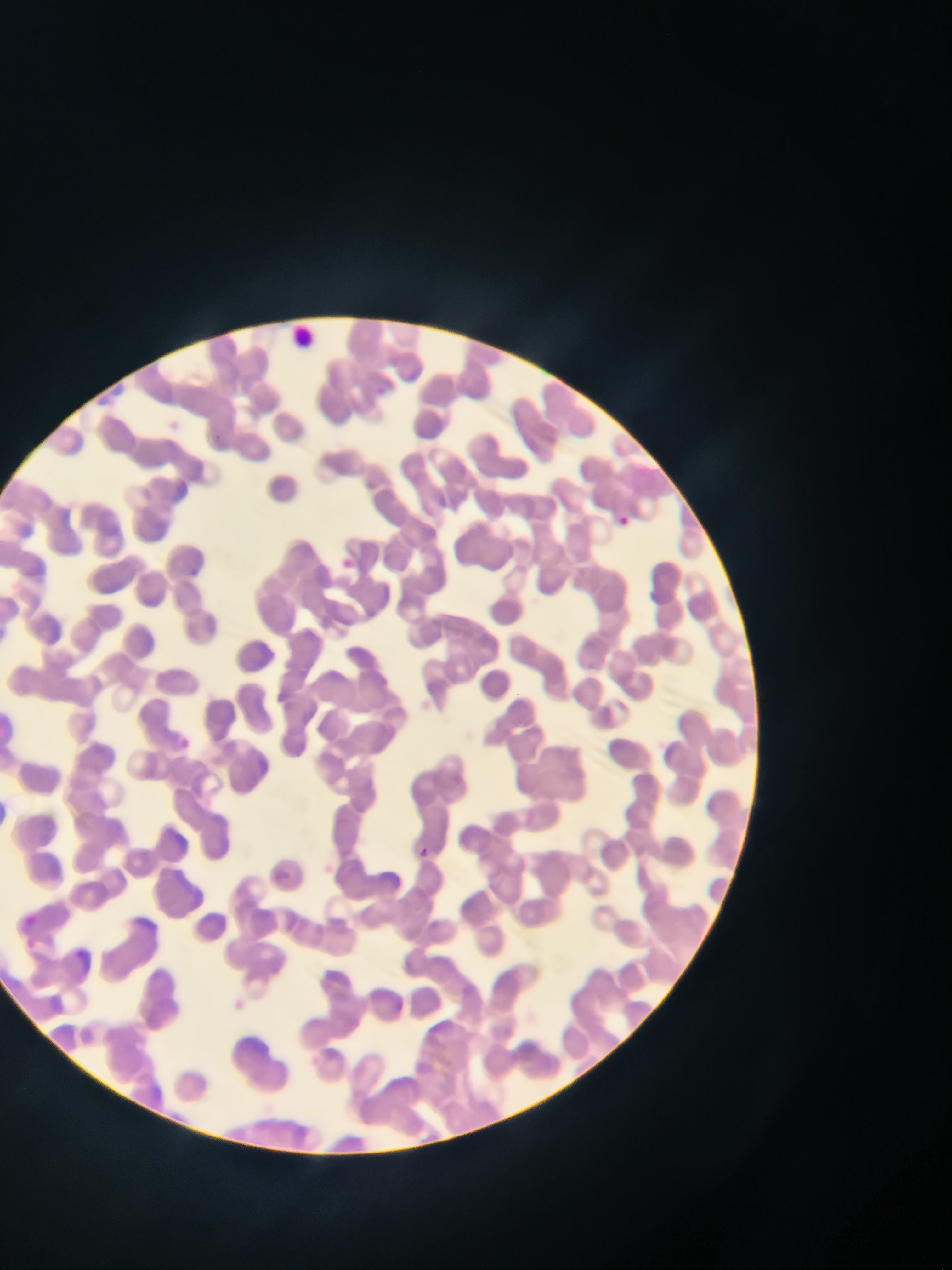

{
  "malaria_parasite_locations": "approximate bounding boxes as {left, top, right, bottom} in pixels: {215, 434, 224, 441}, {620, 510, 638, 525}, {336, 552, 366, 573}, {180, 735, 195, 750}, {416, 849, 438, 864}, {276, 864, 288, 876}",
  "leukocyte_locations": "approximate bounding boxes as {left, top, right, bottom} in pixels: {286, 322, 316, 355}",
  "field_of_view": "single",
  "country": "Ghana",
  "preparation": "thin blood film",
  "capture": "mobile-phone photograph through a microscope",
  "image_size": "952×1270 pixels"
}